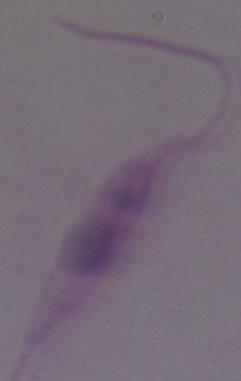

modality = photomicrograph
identification = Leishmania
magnification = 1000x